Assess the morphology of the erythrocytes.
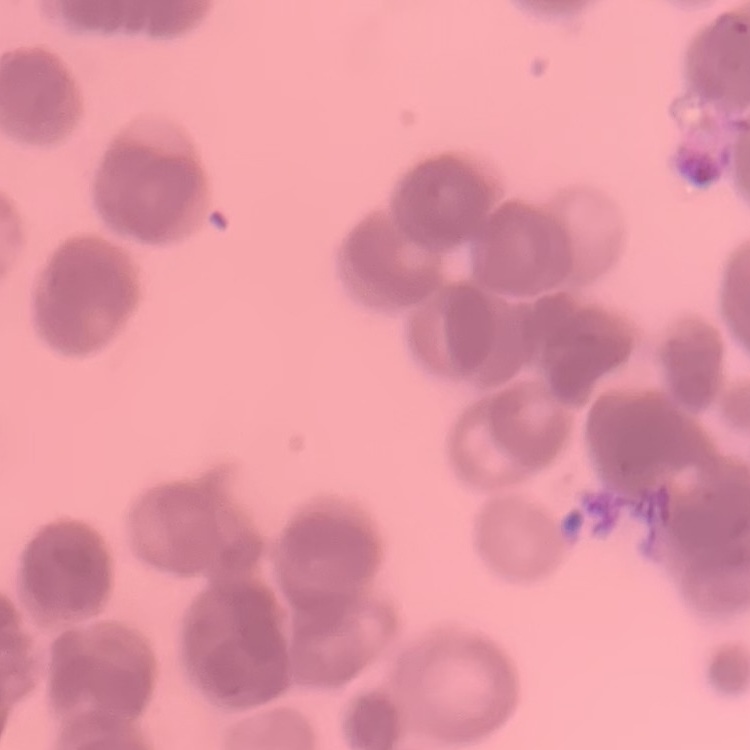
Rouleaux formation.

Summary:
  - Preparation: thin blood film
  - Stain: Field's or Giemsa
  - Image type: one tile cut from a larger photomicrograph